Identify the parasite.
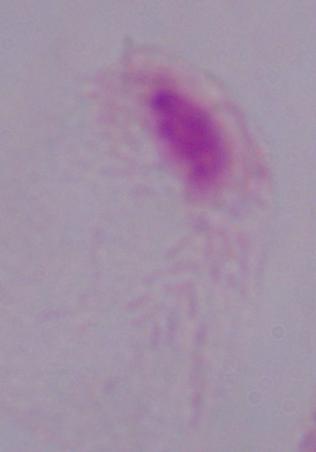
This is a trichomonad.

Micrograph. 1000x magnification.